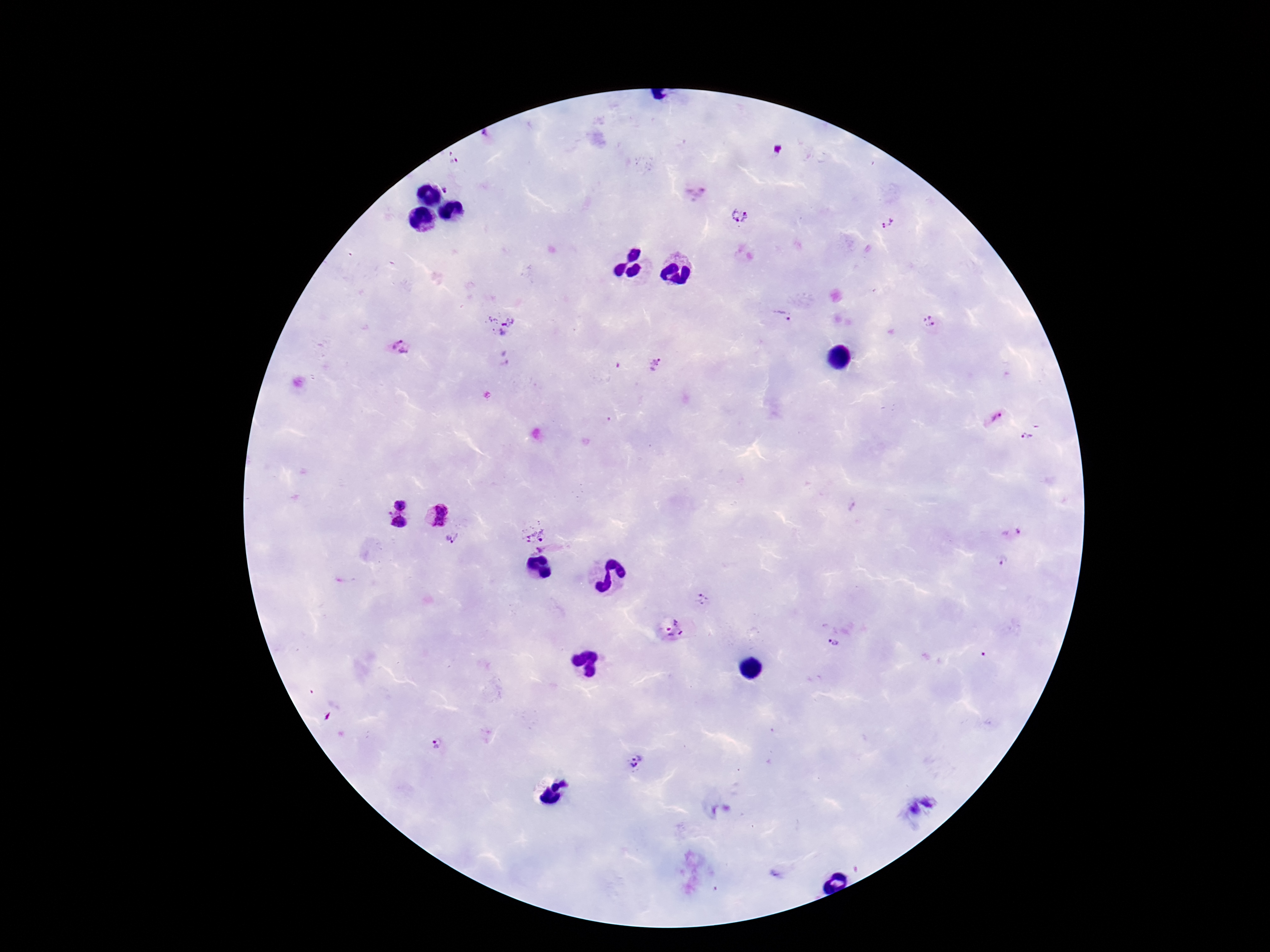
{
  "patient_malaria_status": "infected",
  "capture": "smartphone camera through the microscope eyepiece",
  "plasmodium_parasite_locations": "approximate centers as (x, y) in pixels: (455, 162), (447, 188), (695, 191), (739, 216), (887, 223), (782, 315), (930, 321), (496, 326), (399, 347), (655, 365), (993, 419), (1027, 437), (398, 502), (436, 515), (399, 522), (534, 530), (1012, 534), (453, 538), (542, 551), (1002, 563), (701, 600), (671, 629), (835, 644), (437, 742), (632, 763)",
  "magnification": "100x",
  "stain": "Giemsa",
  "image_size": "1270×952 pixels",
  "preparation": "thick blood smear",
  "field_of_view": "one from this slide"
}